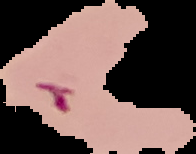
result: malaria parasites detected
preparation: thin blood smear
image_type: segmented cell region with the area outside set to black
image_size: 196×154 pixels